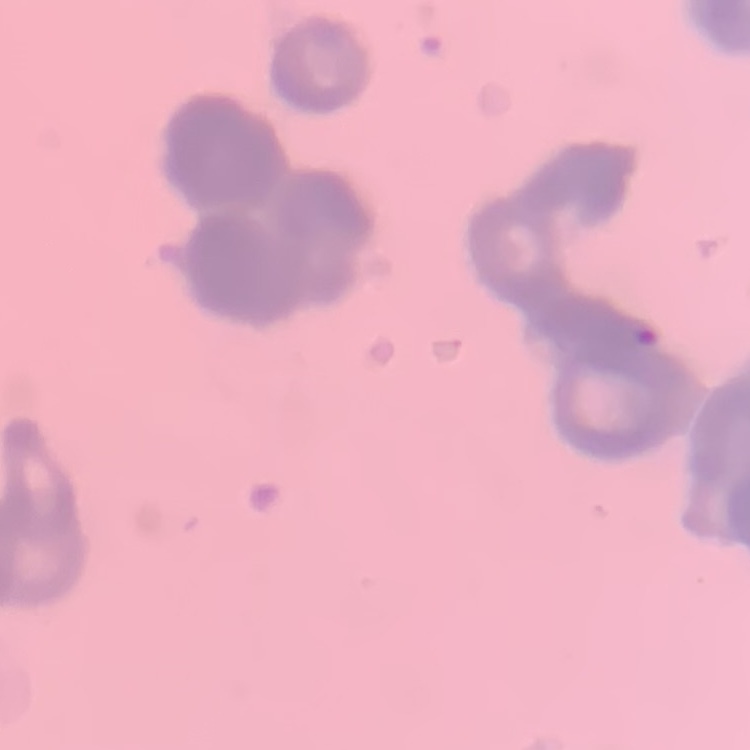
{
  "erythrocyte_morphology": "rouleaux formation",
  "image_type": "square crop of a larger photomicrograph",
  "stain": "Field's or Giemsa",
  "preparation": "thin peripheral smear"
}